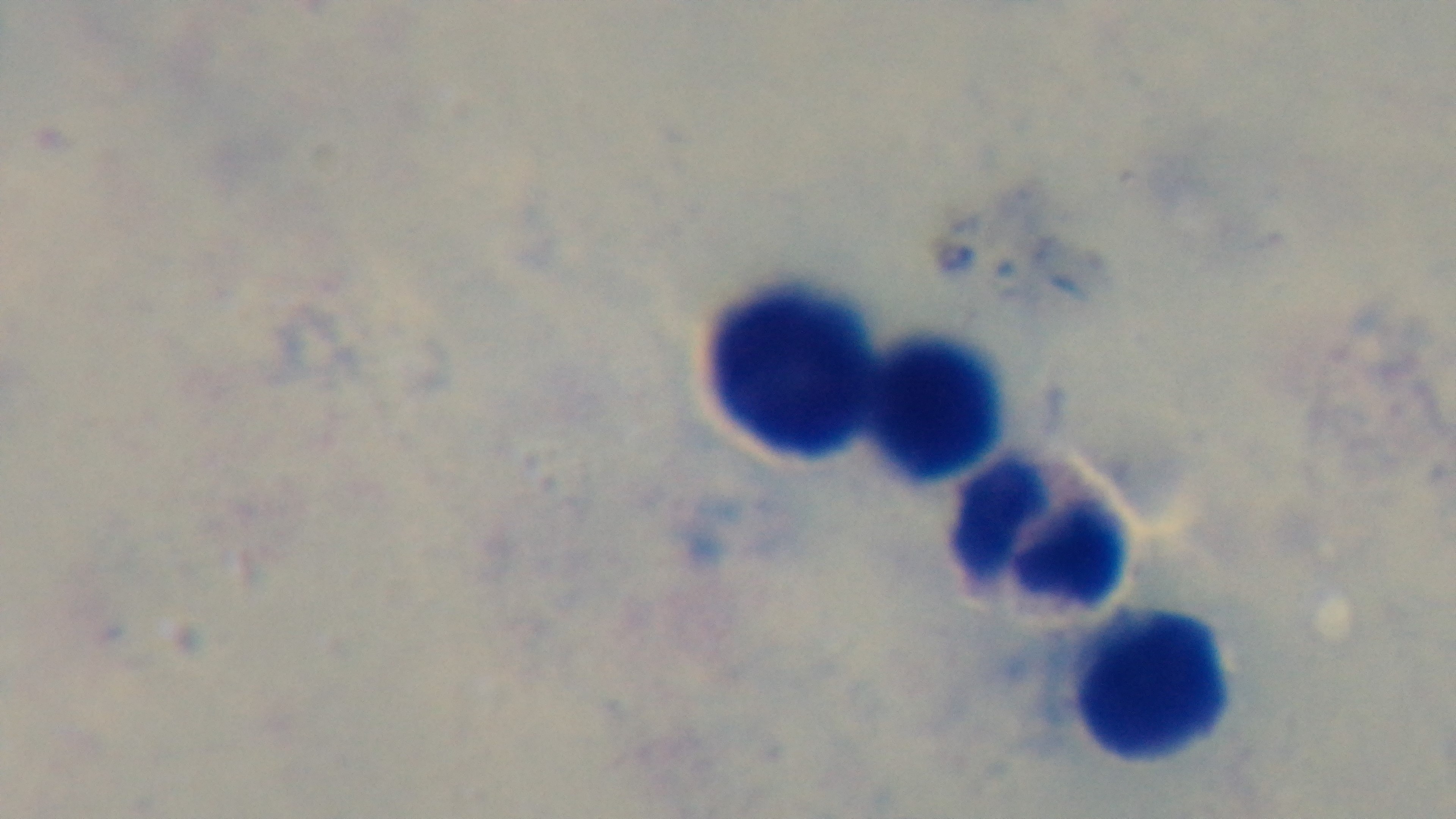

{
  "field_of_view": "one from the slide",
  "objective": "100x oil immersion",
  "capture": "mounted 4K digital camera",
  "stain": "Giemsa",
  "modality": "light microscopy",
  "malaria_status": "uninfected",
  "preparation": "thick smear"
}